Report the malaria status of this cell.
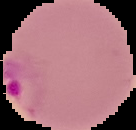

It is parasitized.

Summary:
  - Image type: cell region segmented out of the field of view; surrounding area masked to black
  - Preparation: thin blood film
  - Image size: 136×130 pixels